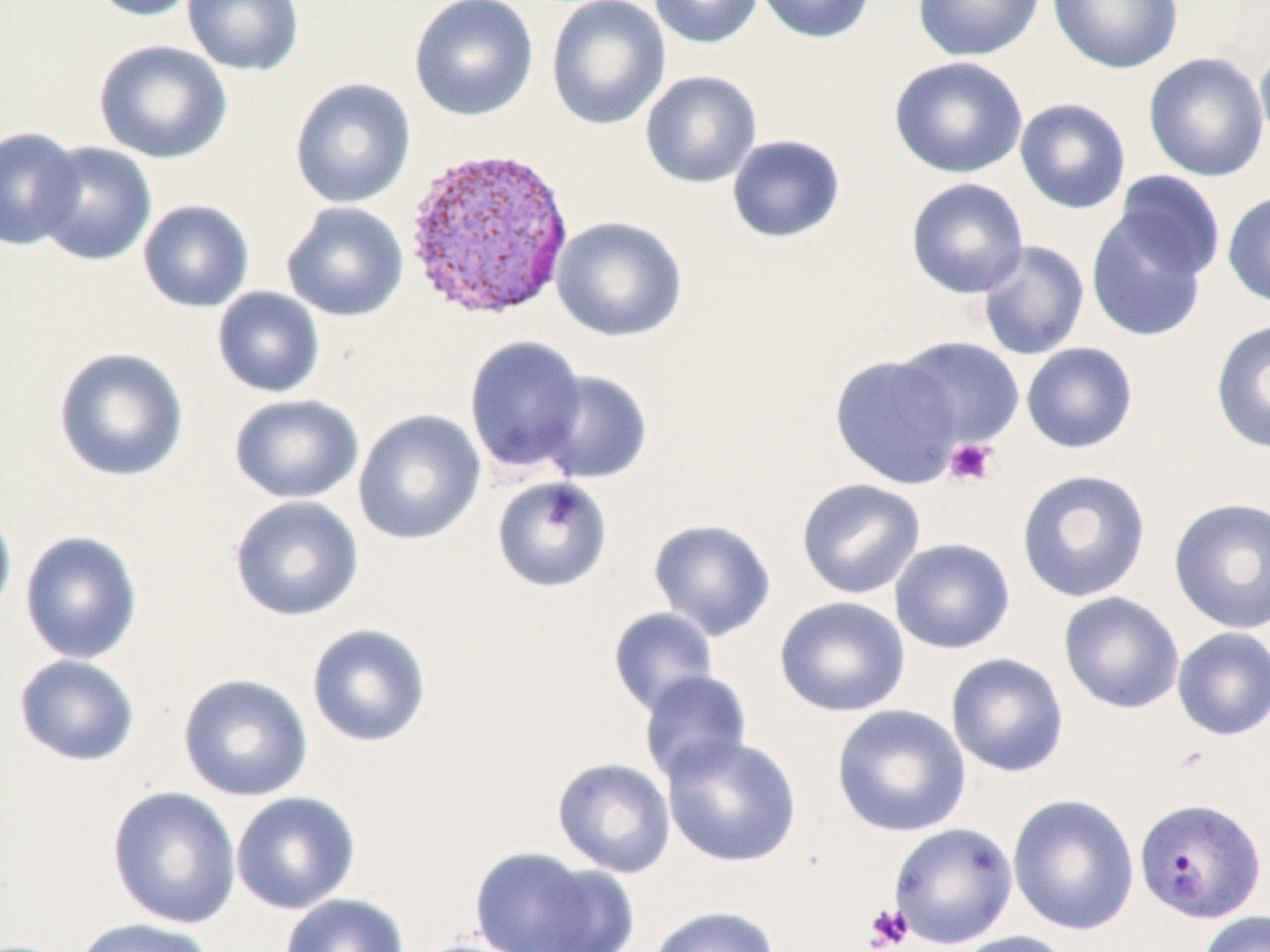

slide-level diagnosis = Plasmodium vivax
modality = optical microscopy
field of view = one of a larger specimen
stain = May-Grünwald-Giemsa
Plasmodium vivax-infected red blood cell locations = approximate bounding boxes as (x1, y1, x2, y2) in pixels: (401, 144, 577, 322), (1133, 796, 1266, 924)
image size = 1270×952 pixels
magnification = 1000x
uninfected red blood cell locations = approximate bounding boxes as (x1, y1, x2, y2) in pixels: (86, 0, 207, 22), (182, 0, 304, 76), (409, 0, 539, 121), (545, 0, 671, 131), (648, 0, 764, 50), (753, 0, 878, 44), (913, 0, 1045, 61), (1048, 0, 1183, 74), (93, 39, 232, 164), (1254, 42, 1270, 157), (1143, 51, 1270, 182), (888, 56, 1028, 179), (640, 69, 762, 189), (289, 78, 416, 209), (1014, 97, 1132, 215), (0, 126, 83, 251), (726, 134, 846, 244), (32, 141, 157, 266), (1112, 170, 1227, 282), (905, 177, 1029, 298), (1222, 190, 1270, 308), (138, 199, 254, 313), (281, 201, 409, 322), (1085, 211, 1211, 343), (551, 215, 688, 342), (975, 239, 1090, 361), (212, 286, 325, 398), (1210, 319, 1270, 453), (463, 334, 589, 475), (894, 336, 1026, 450), (1020, 341, 1139, 454), (53, 346, 189, 482), (829, 353, 965, 489), (536, 369, 654, 485), (228, 393, 364, 504), (353, 409, 486, 545), (1015, 468, 1152, 603), (491, 476, 613, 593), (795, 478, 927, 600), (228, 495, 364, 622), (1168, 496, 1270, 634), (0, 500, 17, 631), (647, 517, 778, 642), (19, 531, 143, 664), (889, 537, 1016, 655), (1058, 591, 1185, 715), (773, 595, 911, 718), (607, 606, 720, 716), (306, 623, 432, 748), (1171, 627, 1270, 741), (945, 652, 1070, 778), (13, 654, 140, 767), (638, 669, 753, 786), (177, 673, 314, 801), (830, 703, 972, 838), (662, 735, 803, 868), (551, 756, 676, 878), (106, 785, 241, 929), (231, 791, 360, 914), (1007, 793, 1140, 936), (887, 822, 1018, 949), (468, 846, 618, 952), (279, 893, 410, 952), (647, 904, 781, 952), (1197, 910, 1270, 952), (70, 917, 217, 952), (946, 930, 1076, 952)
platelet locations = approximate bounding boxes as (x1, y1, x2, y2) in pixels: (944, 437, 999, 487), (863, 903, 913, 951)
preparation = thin blood film